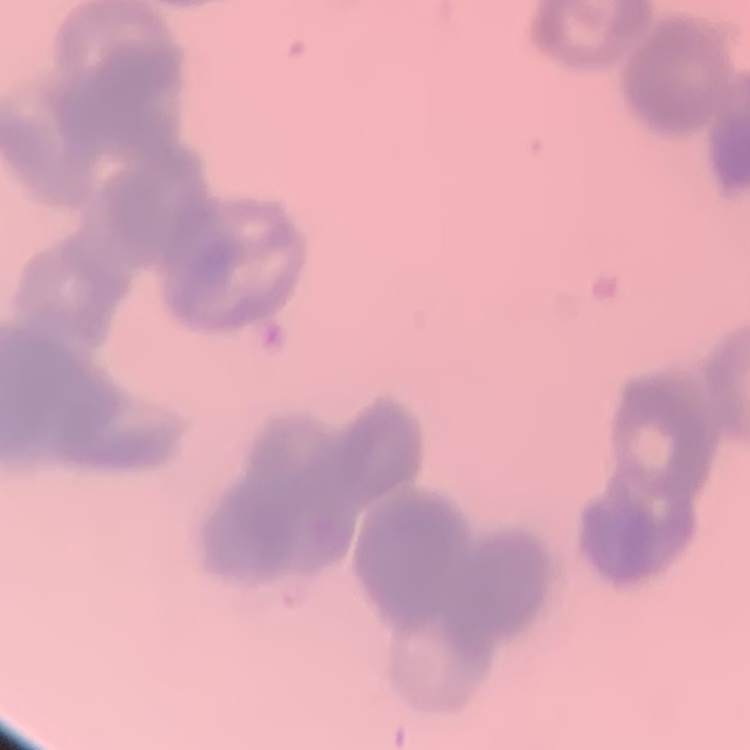

The erythrocytes show rouleaux formation. Stained with either Field's or Giemsa. Thin blood smear. One tile cut from a larger photomicrograph.